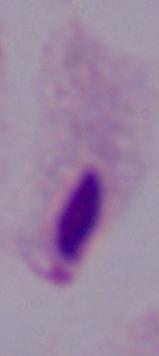
{
  "identification": "trichomonad",
  "magnification": "1000x",
  "modality": "photomicrograph"
}